Classify this cell by malaria status.
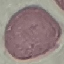
It is uninfected.

Cell patch, automatically extracted from a larger field of view and resized to 64 × 64 pixels. Thin smear of blood. Giemsa stain. Acquired by smartphone through the microscope eyepiece.